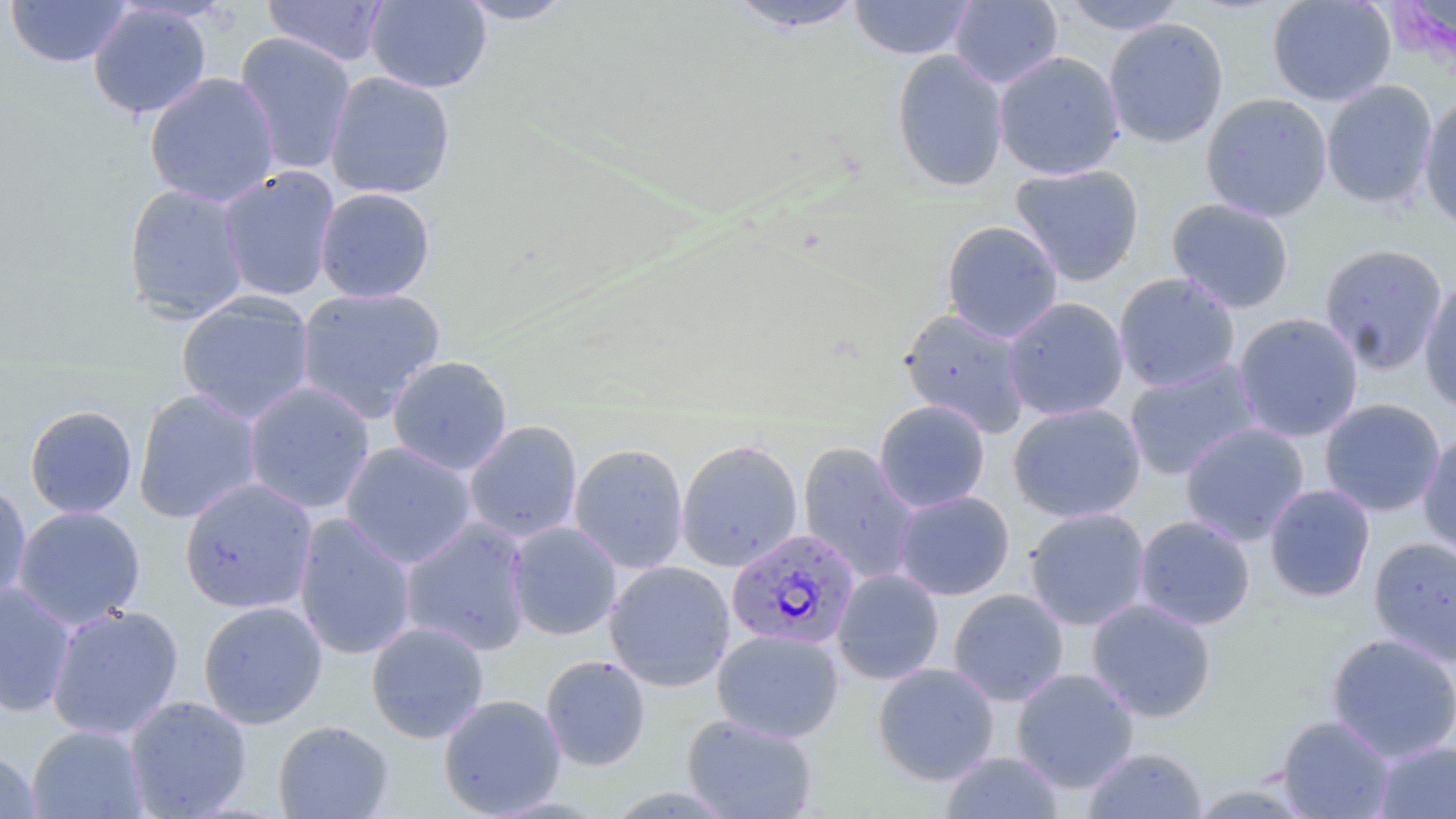

slide-level diagnosis = Plasmodium falciparum
magnification = 1000x
preparation = thin blood smear
modality = optical microscopy
field of view = single
image size = 1456×819 pixels
stain = May-Grünwald-Giemsa
uninfected red blood cell locations = approximate bounding boxes as (x1,y1)-(x2,y2) corner pairs in pixels: (5,0)-(131,68), (261,0)-(390,66), (457,0)-(574,24), (724,0)-(868,33), (849,0)-(975,60), (949,0)-(1063,89), (1060,0)-(1186,36), (1266,0)-(1397,106), (365,1)-(492,93), (87,3)-(212,119), (1103,17)-(1228,149), (234,31)-(357,175), (891,49)-(1009,192), (993,51)-(1125,180), (325,70)-(456,200), (144,71)-(281,208), (1321,81)-(1438,209), (1201,93)-(1333,222), (1419,94)-(1456,231), (1009,164)-(1145,286), (218,166)-(340,302), (123,183)-(249,323), (314,187)-(436,304), (1166,197)-(1295,314), (941,220)-(1064,343), (1319,243)-(1449,374), (1114,272)-(1241,393), (1419,278)-(1456,413), (295,286)-(446,420), (176,292)-(316,424), (1003,297)-(1129,421), (898,307)-(1032,437), (1233,313)-(1364,443), (386,355)-(513,476), (1124,359)-(1262,480), (243,381)-(376,514), (133,388)-(264,524), (1319,398)-(1446,517), (874,400)-(990,513), (1007,402)-(1146,523), (24,404)-(138,519), (463,420)-(583,543), (1180,421)-(1310,545), (1418,429)-(1456,560), (676,439)-(803,572), (340,441)-(478,570), (797,442)-(920,585), (569,443)-(689,574), (179,477)-(318,614), (0,481)-(32,607), (1264,484)-(1375,602), (893,490)-(1015,601), (12,505)-(146,630), (1024,508)-(1151,630), (293,513)-(417,660), (1134,514)-(1256,630), (399,518)-(533,656), (505,521)-(623,641), (1368,536)-(1456,666), (603,560)-(735,692), (832,569)-(944,685), (0,582)-(76,719), (948,589)-(1069,707), (1087,598)-(1217,723), (198,600)-(327,728), (46,604)-(184,740), (366,621)-(489,743), (712,629)-(844,743), (1325,632)-(1456,763), (540,655)-(651,771), (872,662)-(1000,785), (1011,668)-(1139,793), (438,693)-(567,818), (124,695)-(252,818), (682,713)-(818,819), (1276,715)-(1396,818), (273,720)-(393,819), (26,724)-(149,819), (1373,741)-(1456,819), (1082,747)-(1207,818), (940,750)-(1065,818), (0,751)-(40,818)
Plasmodium falciparum-infected red blood cell locations = approximate bounding boxes as (x1,y1)-(x2,y2) corner pairs in pixels: (728,528)-(866,651)